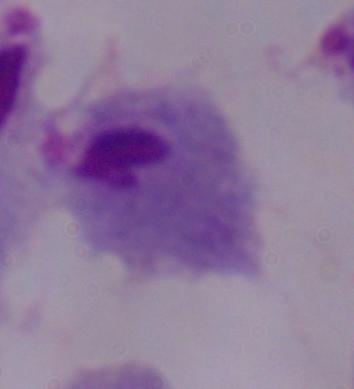
Summary:
  - Magnification: 1000x
  - Identification: trichomonad
  - Modality: photomicrograph